Assess the morphology of the red blood cells.
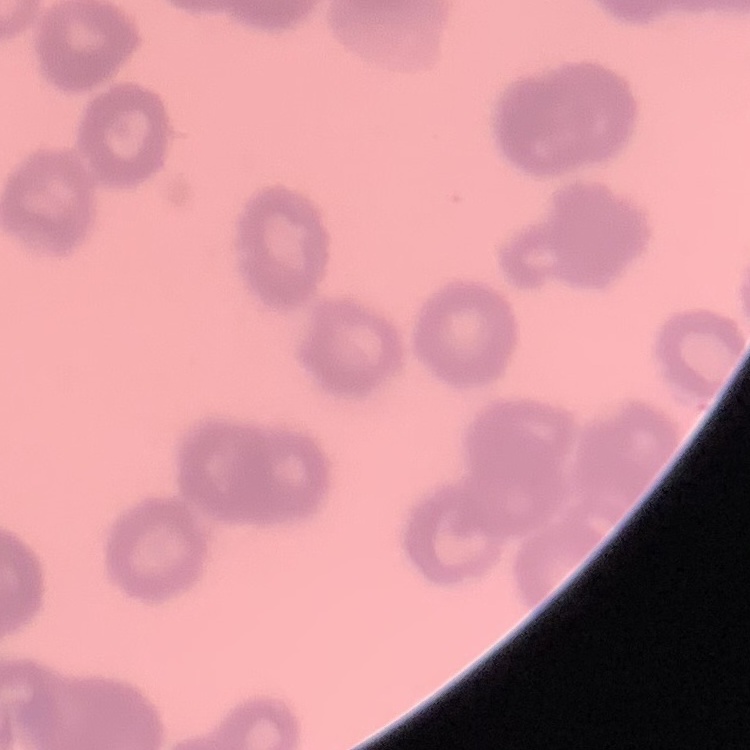
They show rouleaux formation.

Thin peripheral smear. Field's or Giemsa stain. One tile cut from a larger photomicrograph.